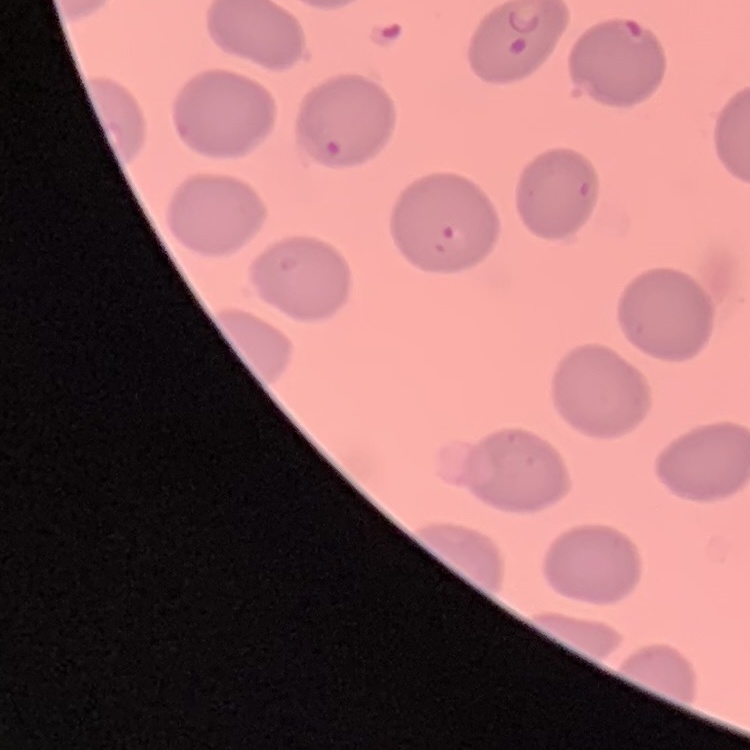
erythrocyte morphology = no rouleaux formation
stain = Field's or Giemsa
preparation = thin blood film
image type = one tile cut from a larger photomicrograph